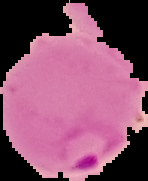
Summary:
  - Image size: 148×181 pixels
  - Image type: cell region segmented out of the field of view; surrounding area masked to black
  - Result: Plasmodium parasites detected
  - Preparation: thin blood smear